State the blood parasite species.
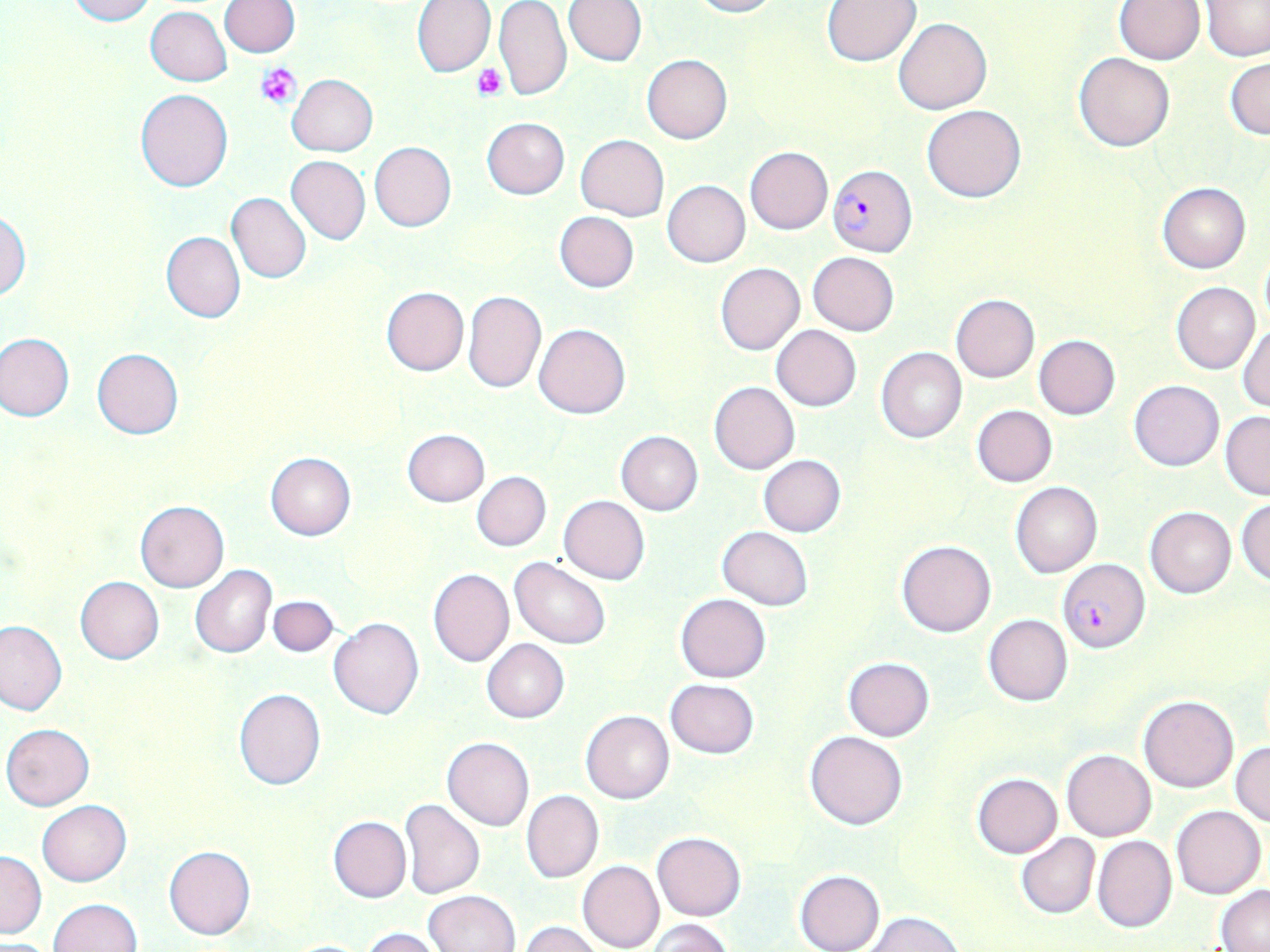

Plasmodium falciparum.

magnification = 1000x
stain = May-Grünwald-Giemsa
field of view = single
image size = 1270×952 pixels
platelet locations = approximate bounding boxes as [x1, y1, x2, y2] in pixels: [257, 63, 302, 108], [472, 63, 508, 100]
Plasmodium falciparum-infected red blood cell locations = approximate bounding boxes as [x1, y1, x2, y2] in pixels: [829, 164, 916, 255], [1057, 559, 1150, 652]
modality = light microscopy
uninfected red blood cell locations = approximate bounding boxes as [x1, y1, x2, y2] in pixels: [67, 0, 156, 25], [412, 0, 495, 77], [563, 0, 646, 67], [689, 0, 777, 17], [823, 0, 921, 65], [1115, 0, 1205, 64], [219, 1, 300, 57], [1203, 1, 1270, 61], [495, 3, 572, 102], [146, 6, 231, 86], [894, 17, 992, 115], [1073, 51, 1175, 152], [642, 54, 732, 143], [1226, 57, 1269, 139], [286, 74, 378, 156], [136, 88, 233, 191], [922, 104, 1026, 203], [482, 117, 570, 199], [576, 134, 668, 221], [369, 141, 457, 232], [744, 146, 833, 234], [286, 155, 370, 245], [662, 180, 750, 266], [1158, 183, 1250, 273], [227, 192, 311, 283], [0, 210, 30, 302], [554, 211, 639, 292], [161, 231, 244, 322], [1260, 249, 1270, 328], [807, 252, 900, 337], [715, 263, 804, 355], [1171, 282, 1259, 374], [382, 287, 469, 376], [462, 290, 546, 394], [951, 294, 1039, 382], [534, 322, 630, 418], [1236, 324, 1270, 411], [771, 325, 862, 411], [0, 333, 75, 421], [1033, 335, 1120, 419], [875, 346, 967, 442], [92, 349, 184, 439], [1130, 380, 1224, 470], [709, 381, 799, 475], [971, 405, 1057, 488], [1220, 411, 1270, 500], [402, 429, 490, 506], [615, 430, 703, 515], [266, 452, 356, 540], [758, 455, 846, 536], [472, 471, 550, 551], [1011, 481, 1102, 578], [558, 495, 650, 584], [1235, 498, 1270, 586], [134, 499, 229, 592], [1145, 506, 1236, 598], [340, 515, 430, 600], [717, 526, 814, 610], [897, 539, 996, 637], [510, 558, 609, 649], [190, 564, 276, 658], [428, 568, 513, 667], [75, 576, 164, 663], [676, 594, 771, 682], [268, 595, 338, 656], [983, 614, 1073, 706], [328, 618, 424, 720], [0, 620, 66, 716], [482, 639, 569, 723], [843, 658, 934, 740], [665, 678, 760, 758], [233, 687, 326, 790], [1137, 694, 1239, 792], [581, 710, 675, 805], [2, 723, 94, 810], [805, 730, 907, 830], [442, 737, 533, 831], [1231, 741, 1269, 828], [1061, 749, 1156, 841], [972, 774, 1062, 858], [521, 790, 604, 884], [399, 798, 484, 899], [37, 800, 131, 885], [1170, 805, 1266, 899], [329, 816, 410, 903], [653, 832, 746, 921], [1016, 833, 1100, 918], [1092, 835, 1177, 933], [164, 845, 255, 940], [0, 851, 46, 938], [577, 860, 664, 952], [794, 869, 885, 952], [1216, 885, 1270, 950], [423, 890, 520, 952], [47, 899, 142, 952], [865, 912, 964, 952], [646, 919, 736, 952], [520, 921, 603, 952], [360, 927, 447, 952], [282, 939, 375, 951]
preparation = thin blood film